Assess this cell for malaria.
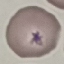
Uninfected.

stain = Giemsa
capture = smartphone camera at the microscope eyepiece
image type = cell patch, automatically extracted from a larger field of view and resized to 64 × 64 pixels
preparation = thin blood smear